Outline each blood parasite and name the species.
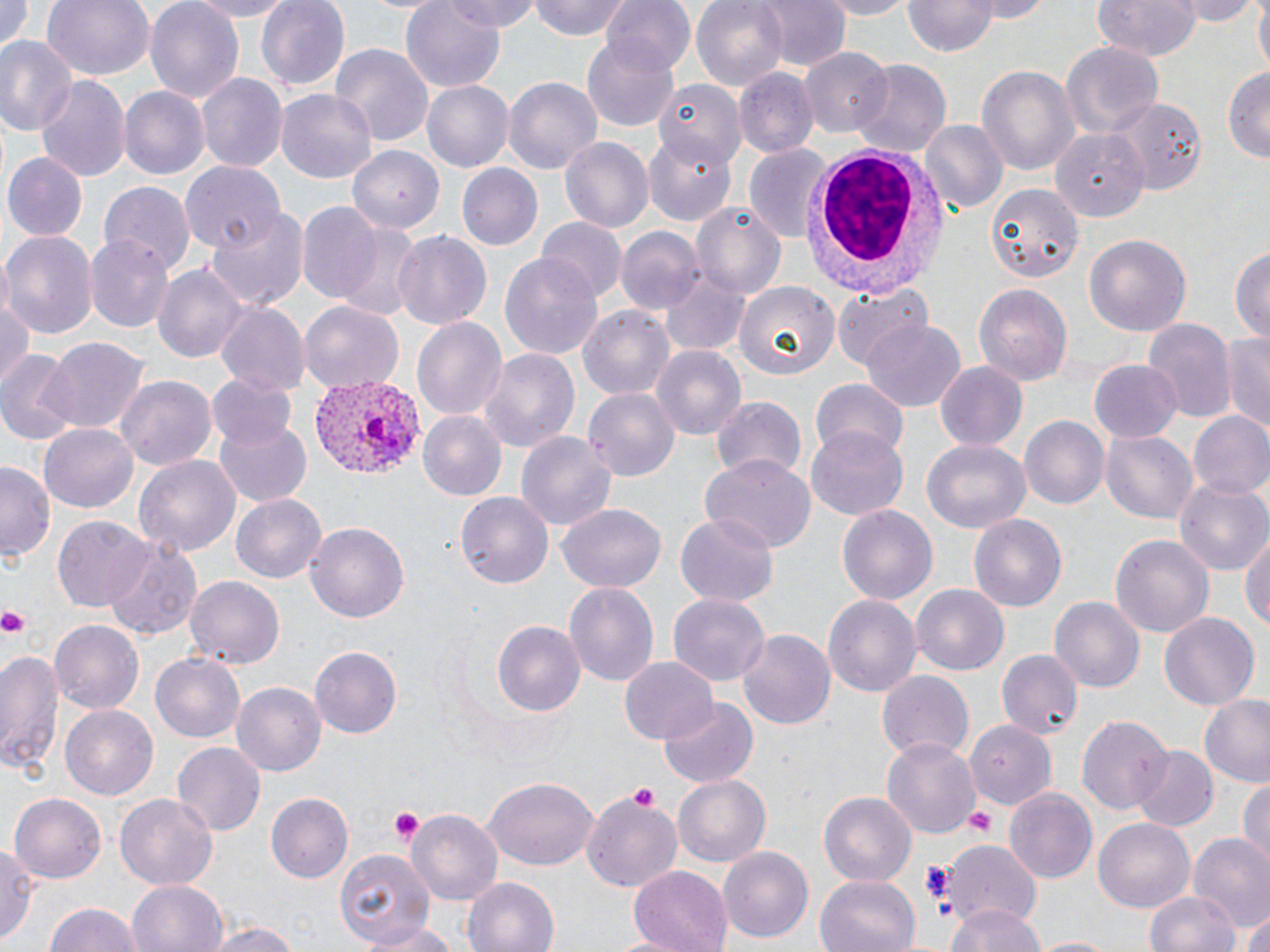
Approximate bounding boxes as named x1/y1/x2/y2 corners in pixels.
Plasmodium vivax-infected red blood cells: (x1=311, y1=378, x2=421, y2=479).
No Plasmodium falciparum, Plasmodium ovale, Plasmodium malariae, Babesia divergens, or Trypanosoma brucei observed.

Summary:
  - Uninfected red blood cell locations: (x1=0, y1=0, x2=34, y2=54), (x1=41, y1=0, x2=155, y2=82), (x1=144, y1=0, x2=245, y2=103), (x1=180, y1=0, x2=297, y2=20), (x1=256, y1=0, x2=351, y2=92), (x1=402, y1=0, x2=505, y2=89), (x1=445, y1=0, x2=539, y2=31), (x1=529, y1=0, x2=632, y2=42), (x1=599, y1=0, x2=694, y2=76), (x1=692, y1=0, x2=789, y2=92), (x1=756, y1=0, x2=850, y2=72), (x1=817, y1=0, x2=916, y2=18), (x1=964, y1=0, x2=1053, y2=23), (x1=1092, y1=0, x2=1200, y2=59), (x1=1175, y1=0, x2=1260, y2=25), (x1=1250, y1=0, x2=1270, y2=74), (x1=904, y1=2, x2=999, y2=57), (x1=773, y1=15, x2=872, y2=125), (x1=581, y1=32, x2=679, y2=130), (x1=0, y1=36, x2=76, y2=139), (x1=1057, y1=41, x2=1166, y2=141), (x1=329, y1=43, x2=436, y2=149), (x1=800, y1=49, x2=891, y2=138), (x1=851, y1=60, x2=950, y2=158), (x1=1222, y1=64, x2=1270, y2=164), (x1=977, y1=65, x2=1078, y2=178), (x1=734, y1=69, x2=818, y2=158), (x1=198, y1=73, x2=287, y2=174), (x1=37, y1=75, x2=131, y2=182), (x1=421, y1=77, x2=514, y2=170), (x1=504, y1=77, x2=603, y2=174), (x1=651, y1=77, x2=750, y2=165), (x1=120, y1=87, x2=209, y2=181), (x1=277, y1=90, x2=376, y2=186), (x1=1108, y1=99, x2=1204, y2=195), (x1=918, y1=121, x2=1007, y2=217), (x1=1050, y1=126, x2=1152, y2=215), (x1=643, y1=134, x2=735, y2=225), (x1=559, y1=136, x2=653, y2=234), (x1=348, y1=144, x2=439, y2=231), (x1=742, y1=147, x2=834, y2=243), (x1=1, y1=152, x2=87, y2=242), (x1=178, y1=161, x2=283, y2=253), (x1=455, y1=162, x2=542, y2=250), (x1=100, y1=180, x2=195, y2=277), (x1=986, y1=187, x2=1079, y2=280), (x1=691, y1=201, x2=787, y2=296), (x1=296, y1=202, x2=383, y2=304), (x1=203, y1=206, x2=309, y2=312), (x1=327, y1=218, x2=422, y2=318), (x1=537, y1=218, x2=625, y2=305), (x1=616, y1=226, x2=704, y2=315), (x1=1, y1=229, x2=97, y2=339), (x1=389, y1=230, x2=493, y2=334), (x1=1083, y1=232, x2=1192, y2=340), (x1=87, y1=234, x2=176, y2=331), (x1=1231, y1=246, x2=1269, y2=346), (x1=500, y1=250, x2=605, y2=360), (x1=154, y1=263, x2=247, y2=365), (x1=660, y1=271, x2=752, y2=357), (x1=835, y1=281, x2=935, y2=368), (x1=973, y1=282, x2=1072, y2=382), (x1=736, y1=283, x2=837, y2=381), (x1=0, y1=290, x2=33, y2=388), (x1=299, y1=301, x2=402, y2=392), (x1=213, y1=302, x2=308, y2=397), (x1=579, y1=305, x2=675, y2=400), (x1=411, y1=315, x2=508, y2=423), (x1=862, y1=316, x2=966, y2=410), (x1=1143, y1=321, x2=1233, y2=421), (x1=1220, y1=332, x2=1270, y2=434), (x1=36, y1=335, x2=152, y2=435), (x1=650, y1=346, x2=747, y2=442), (x1=477, y1=347, x2=581, y2=454), (x1=1, y1=354, x2=78, y2=444), (x1=1089, y1=358, x2=1184, y2=441), (x1=933, y1=362, x2=1028, y2=451), (x1=204, y1=371, x2=297, y2=450), (x1=116, y1=374, x2=215, y2=474), (x1=809, y1=378, x2=909, y2=460), (x1=583, y1=387, x2=680, y2=482), (x1=711, y1=395, x2=807, y2=482), (x1=419, y1=410, x2=507, y2=501), (x1=1188, y1=411, x2=1270, y2=501), (x1=213, y1=412, x2=312, y2=505), (x1=1019, y1=416, x2=1108, y2=509), (x1=39, y1=424, x2=139, y2=514), (x1=804, y1=427, x2=909, y2=520), (x1=1100, y1=429, x2=1197, y2=524), (x1=517, y1=430, x2=616, y2=532), (x1=921, y1=440, x2=1030, y2=537), (x1=133, y1=452, x2=241, y2=558), (x1=701, y1=455, x2=814, y2=554), (x1=1, y1=459, x2=56, y2=565), (x1=1172, y1=478, x2=1269, y2=576), (x1=231, y1=491, x2=327, y2=581), (x1=456, y1=491, x2=554, y2=588), (x1=557, y1=504, x2=667, y2=591), (x1=836, y1=505, x2=938, y2=605), (x1=52, y1=513, x2=154, y2=611), (x1=675, y1=514, x2=778, y2=604), (x1=968, y1=514, x2=1067, y2=612), (x1=304, y1=520, x2=410, y2=622), (x1=1240, y1=528, x2=1270, y2=637), (x1=1110, y1=535, x2=1214, y2=638), (x1=104, y1=539, x2=205, y2=641), (x1=185, y1=574, x2=284, y2=669), (x1=564, y1=581, x2=659, y2=688), (x1=911, y1=583, x2=1008, y2=675), (x1=669, y1=592, x2=770, y2=686), (x1=823, y1=593, x2=920, y2=700), (x1=1051, y1=596, x2=1143, y2=695), (x1=1158, y1=611, x2=1260, y2=711), (x1=489, y1=618, x2=585, y2=716), (x1=49, y1=620, x2=145, y2=715), (x1=737, y1=628, x2=836, y2=733), (x1=308, y1=645, x2=403, y2=739), (x1=1, y1=647, x2=65, y2=776), (x1=996, y1=649, x2=1082, y2=741), (x1=151, y1=652, x2=244, y2=743), (x1=619, y1=656, x2=717, y2=744), (x1=876, y1=670, x2=974, y2=764), (x1=231, y1=678, x2=326, y2=774), (x1=1199, y1=696, x2=1270, y2=789), (x1=657, y1=699, x2=756, y2=788), (x1=60, y1=705, x2=159, y2=799), (x1=1076, y1=715, x2=1171, y2=815), (x1=966, y1=720, x2=1057, y2=812), (x1=881, y1=737, x2=980, y2=840), (x1=172, y1=740, x2=265, y2=837), (x1=1132, y1=744, x2=1220, y2=831), (x1=674, y1=775, x2=769, y2=867), (x1=484, y1=776, x2=599, y2=874), (x1=1237, y1=780, x2=1269, y2=867), (x1=1005, y1=786, x2=1098, y2=883), (x1=115, y1=790, x2=217, y2=889), (x1=819, y1=791, x2=914, y2=887), (x1=579, y1=792, x2=680, y2=892), (x1=9, y1=793, x2=107, y2=883), (x1=265, y1=794, x2=353, y2=884), (x1=406, y1=809, x2=502, y2=903), (x1=1095, y1=818, x2=1193, y2=914), (x1=1187, y1=835, x2=1270, y2=934), (x1=943, y1=840, x2=1040, y2=931), (x1=0, y1=844, x2=40, y2=948), (x1=718, y1=845, x2=815, y2=942), (x1=335, y1=847, x2=434, y2=949), (x1=628, y1=866, x2=733, y2=951), (x1=816, y1=875, x2=921, y2=952), (x1=463, y1=876, x2=559, y2=952), (x1=128, y1=879, x2=228, y2=952), (x1=1144, y1=888, x2=1243, y2=952), (x1=43, y1=902, x2=149, y2=952), (x1=944, y1=904, x2=1047, y2=952), (x1=1240, y1=912, x2=1270, y2=952), (x1=203, y1=919, x2=307, y2=952), (x1=353, y1=920, x2=471, y2=950), (x1=1025, y1=936, x2=1125, y2=952)
  - White blood cell locations: (x1=800, y1=140, x2=951, y2=296)
  - Platelet locations: (x1=0, y1=605, x2=33, y2=639), (x1=627, y1=782, x2=665, y2=813), (x1=963, y1=806, x2=998, y2=839), (x1=385, y1=807, x2=426, y2=844), (x1=919, y1=859, x2=951, y2=901)
  - Slide-level diagnosis: Plasmodium vivax
  - Modality: light microscopy
  - Preparation: thin blood film
  - Image size: 1270×952 pixels
  - Stain: May-Grünwald-Giemsa
  - Field of view: one of a larger specimen
  - Magnification: 1000x